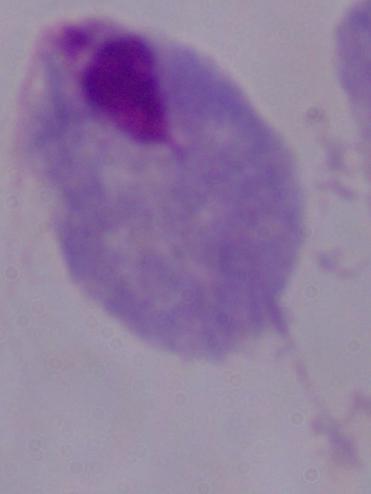

Summary:
  - Modality: photomicrograph
  - Magnification: 1000x
  - Identification: trichomonad